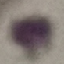

{
  "malaria_status": "uninfected",
  "image_type": "cell patch, automatically extracted from a larger field of view and resized to 64 × 64 pixels",
  "preparation": "thin smear",
  "capture": "smartphone through the microscope eyepiece",
  "stain": "Giemsa"
}